Give the position of every leukocyte visible.
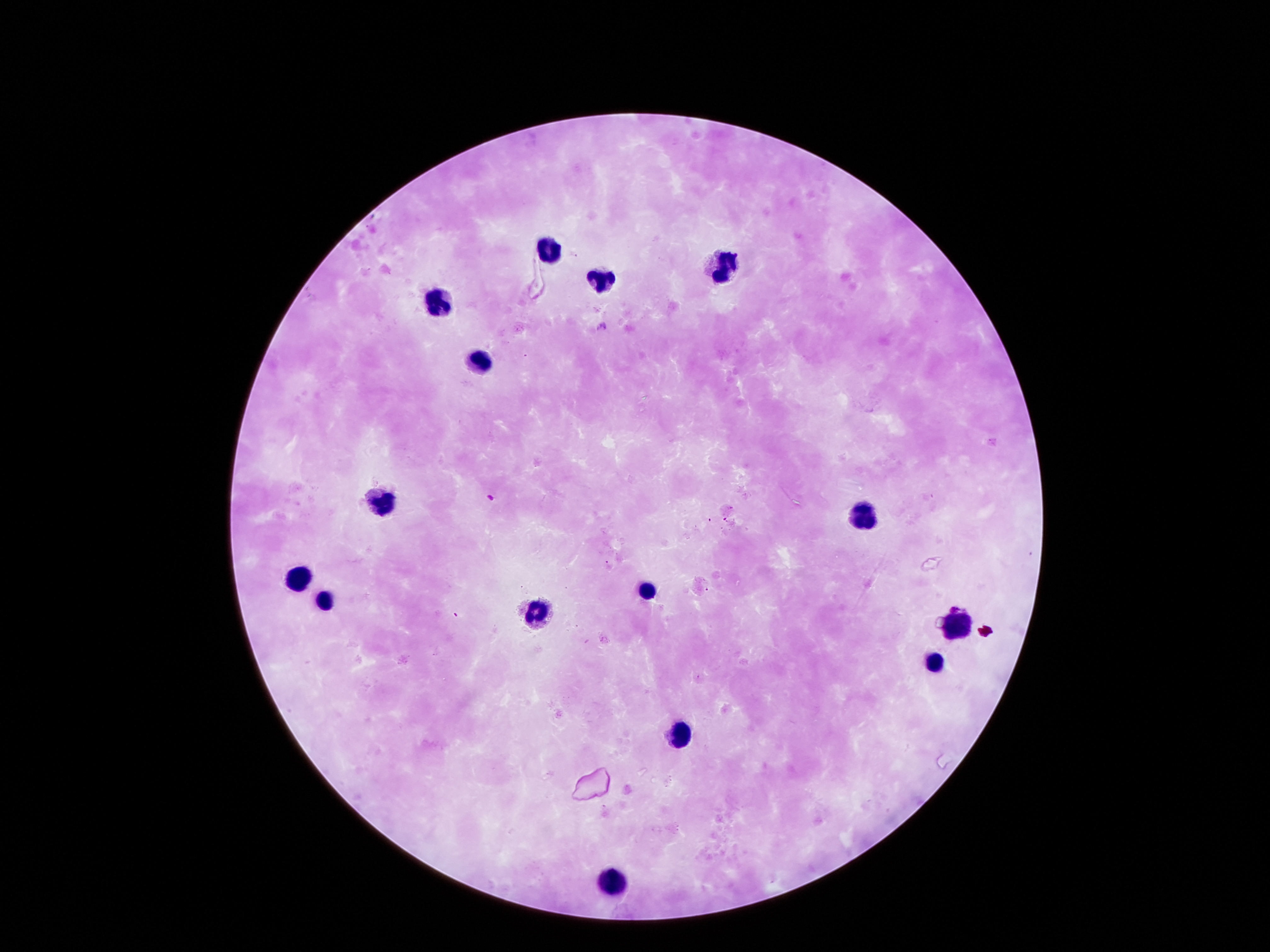

Approximate centers as (x, y) in pixels.
Leukocytes: (548, 249), (722, 266), (597, 282), (435, 303), (480, 359), (383, 502), (865, 511), (293, 576), (642, 589), (322, 597), (535, 613), (949, 621), (936, 660), (681, 731), (613, 876).

Giemsa stain. Patient malaria status: negative. Image is 1270×952 pixels. One field from this slide. Thick blood film. 100x magnification. Photographed through the microscope eyepiece with a smartphone camera.